Locate every blood parasite and identify its species.
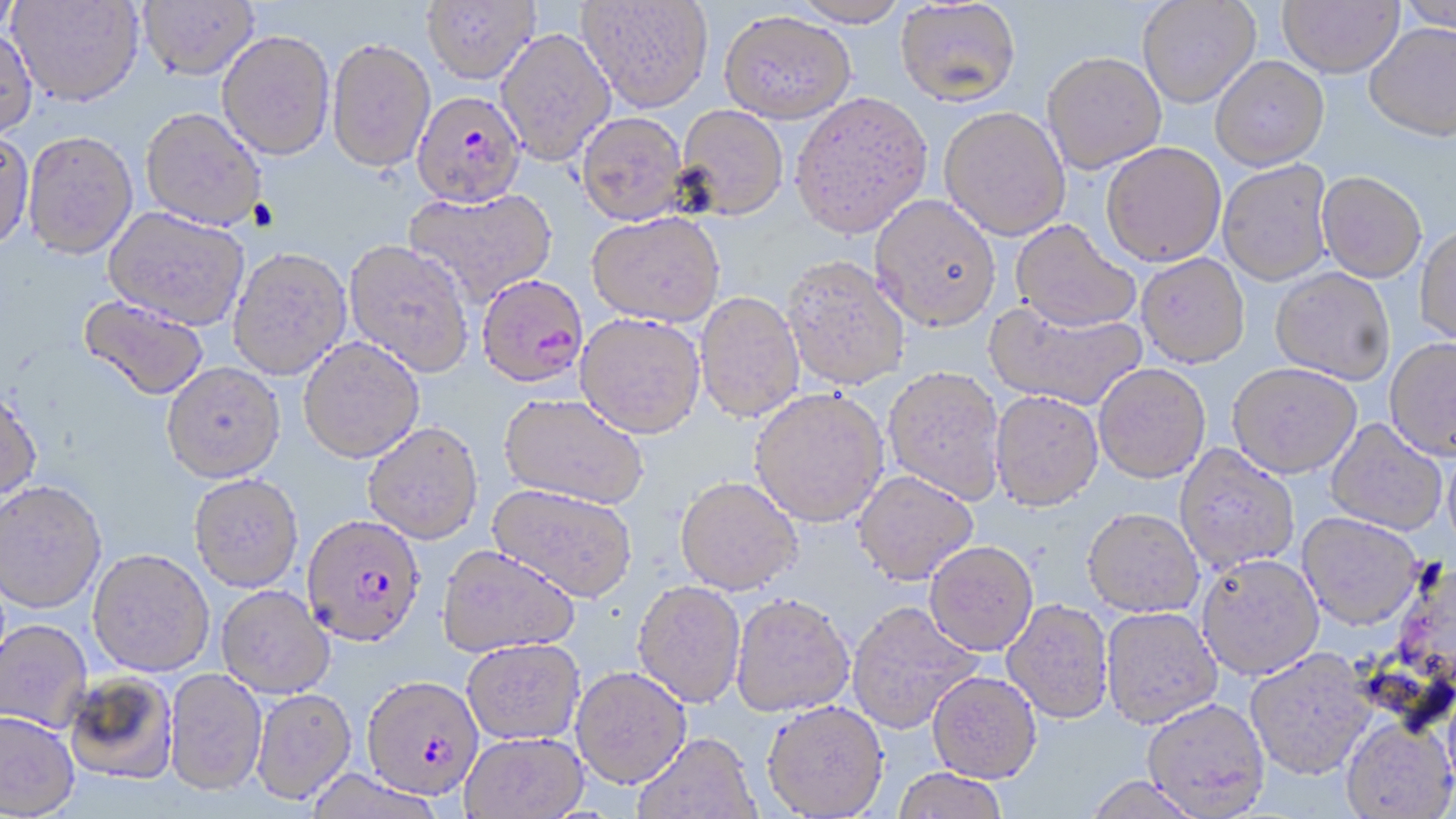

Approximate bounding boxes as [x1, y1, x2, y2] in pixels.
Plasmodium falciparum-infected red blood cells: [411, 90, 526, 208], [476, 273, 589, 388], [300, 521, 422, 648], [361, 675, 485, 802].
No Plasmodium ovale, Plasmodium malariae, Plasmodium vivax, Babesia divergens, or Trypanosoma brucei observed.

{
  "slide_level_diagnosis": "Plasmodium falciparum",
  "modality": "optical microscopy",
  "preparation": "thin blood film",
  "field_of_view": "single",
  "uninfected_red_blood_cell_locations": "approximate bounding boxes as [x1, y1, x2, y2] in pixels: [0, 0, 20, 43], [138, 0, 258, 80], [422, 0, 539, 84], [578, 0, 713, 112], [790, 0, 909, 27], [1137, 0, 1261, 108], [1278, 0, 1403, 77], [1398, 0, 1456, 35], [8, 1, 144, 106], [895, 1, 1021, 106], [719, 10, 856, 123], [1365, 22, 1456, 140], [0, 27, 38, 139], [495, 27, 616, 166], [217, 30, 335, 160], [327, 37, 436, 172], [1042, 51, 1166, 173], [1210, 55, 1329, 169], [790, 91, 933, 239], [675, 105, 789, 220], [939, 106, 1071, 241], [140, 107, 267, 231], [576, 112, 689, 225], [0, 130, 34, 252], [23, 130, 138, 259], [1101, 142, 1227, 266], [1218, 159, 1334, 285], [1316, 171, 1427, 282], [402, 188, 558, 306], [869, 194, 1001, 331], [104, 206, 249, 330], [587, 211, 726, 326], [1011, 219, 1141, 332], [1414, 225, 1456, 346], [344, 239, 474, 376], [227, 246, 351, 380], [1136, 253, 1250, 367], [780, 254, 910, 390], [1270, 268, 1395, 384], [695, 290, 805, 422], [78, 295, 209, 401], [984, 300, 1147, 410], [575, 312, 706, 438], [1384, 336, 1456, 458], [298, 337, 424, 463], [1227, 361, 1361, 478], [161, 362, 285, 483], [1094, 363, 1211, 483], [883, 365, 1007, 505], [749, 387, 889, 527], [0, 389, 42, 503], [990, 390, 1104, 511], [499, 393, 648, 509], [1326, 418, 1447, 536], [363, 422, 484, 545], [1173, 443, 1300, 573], [1442, 444, 1456, 557], [852, 470, 979, 585], [188, 473, 304, 593], [675, 475, 802, 594], [0, 483, 106, 615], [487, 483, 638, 601], [1082, 507, 1204, 617], [1297, 512, 1423, 630], [924, 541, 1038, 655], [436, 545, 580, 658], [87, 551, 214, 678], [1196, 553, 1324, 679], [632, 580, 746, 708], [217, 586, 335, 699], [730, 593, 855, 717], [1002, 598, 1114, 724], [846, 600, 982, 733], [1100, 607, 1224, 728], [0, 621, 92, 734], [462, 639, 585, 745], [1245, 648, 1376, 780], [570, 666, 692, 789], [163, 669, 268, 799], [927, 670, 1042, 782], [63, 672, 179, 787], [251, 689, 356, 807], [1142, 697, 1270, 816], [762, 699, 890, 818], [0, 713, 79, 818], [1341, 717, 1456, 818], [460, 732, 589, 819], [633, 733, 760, 819], [891, 768, 1009, 819], [1081, 775, 1205, 819]",
  "image_size": "1456×819 pixels",
  "stain": "May-Grünwald-Giemsa",
  "magnification": "1000x"
}